Assess the morphology of the red blood cells.
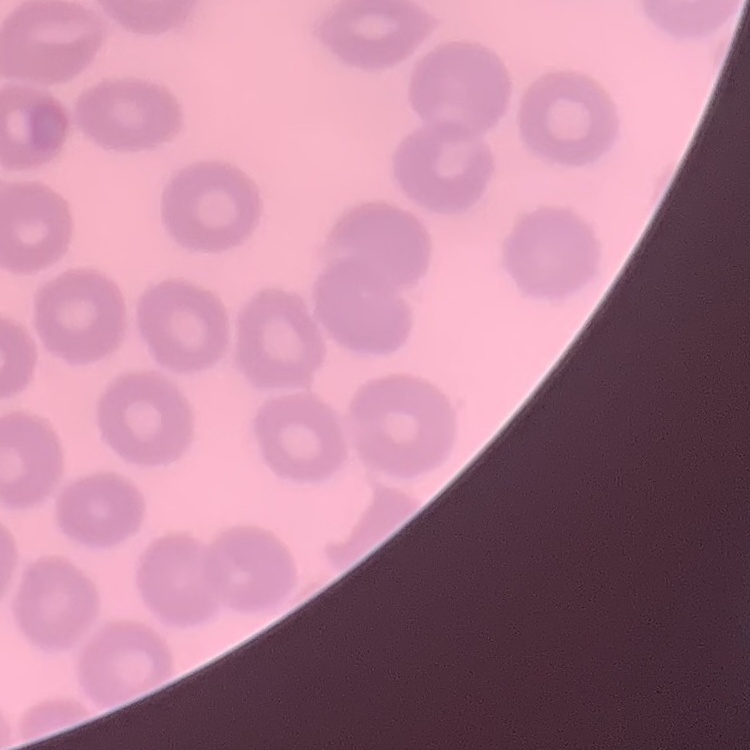
They show no rouleaux formation.

Field's or Giemsa stain. One tile cut from a larger photomicrograph. Thin blood film.